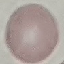

result: no malaria parasites seen
capture: smartphone camera at the microscope eyepiece
preparation: thin smear
stain: Giemsa
image_type: cell patch, automatically extracted from a larger field of view and resized to 64 × 64 pixels